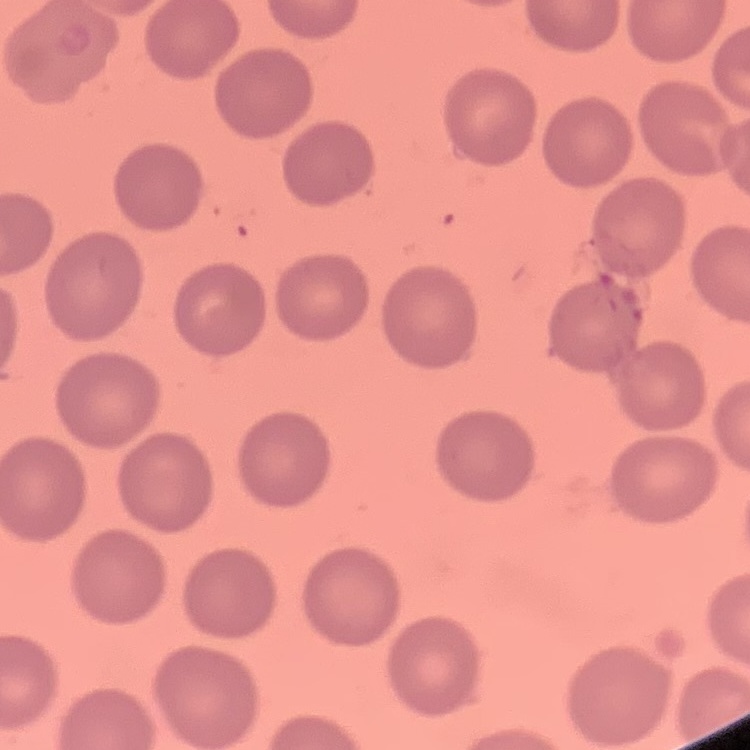
The red blood cells exhibit no rouleaux formation. Thin blood film. Stained with either Field's or Giemsa. Square crop of a larger photomicrograph.